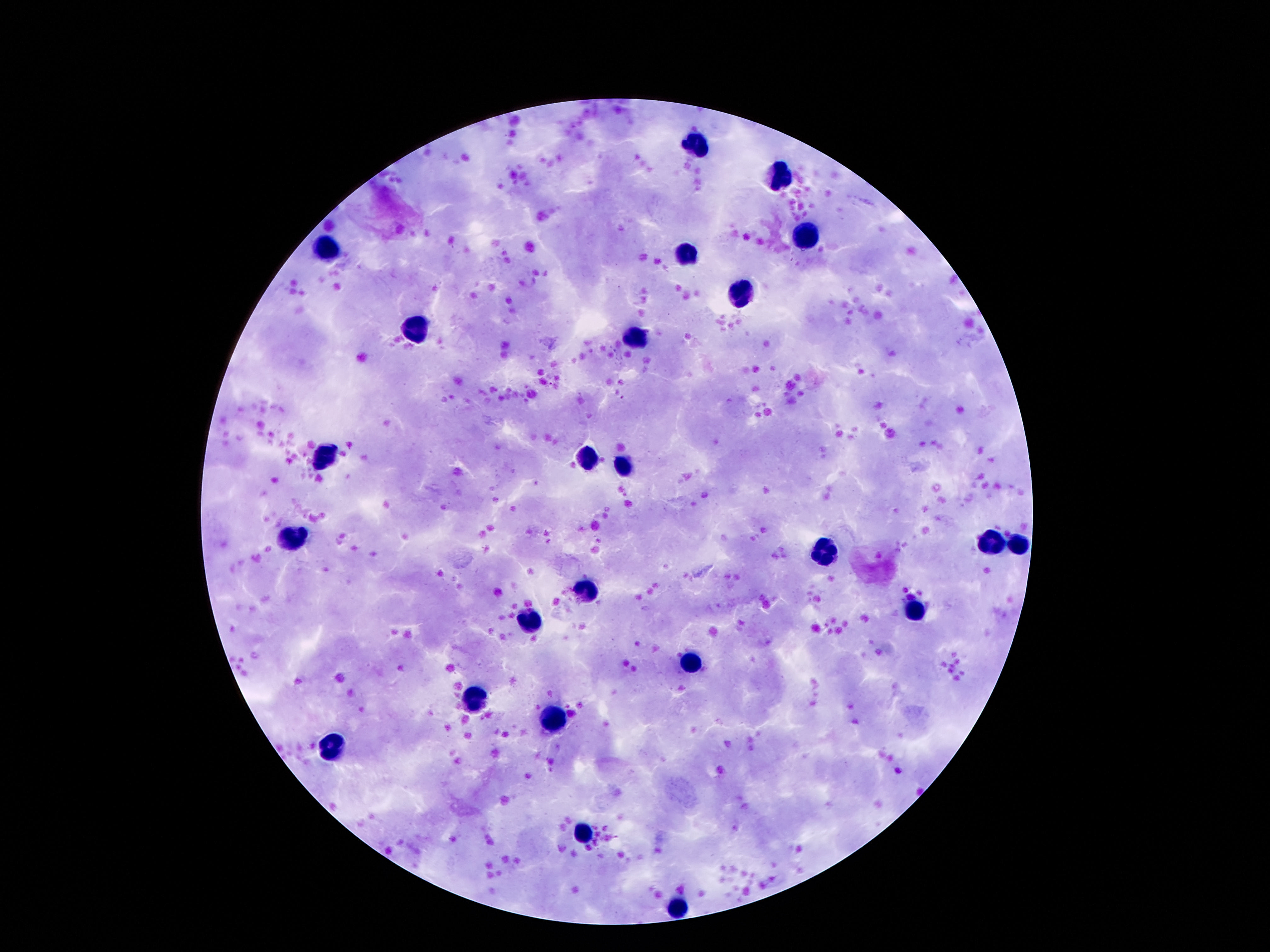

Approximate object centers, in pixels from the top-left corner. Leukocyte locations: (x=694, y=145), (x=773, y=180), (x=808, y=238), (x=323, y=246), (x=683, y=254), (x=743, y=297), (x=412, y=330), (x=637, y=335), (x=325, y=454), (x=588, y=457), (x=624, y=465), (x=290, y=536), (x=995, y=543), (x=1017, y=544), (x=824, y=551), (x=583, y=590), (x=914, y=609), (x=529, y=622), (x=689, y=663), (x=469, y=700), (x=548, y=719), (x=333, y=746), (x=583, y=834), (x=678, y=906). Giemsa-stained preparation. Single field of view. Patient malaria status: uninfected. Image is 1270×952 pixels. 100x magnification. Thick blood film. Smartphone photograph taken through the microscope eyepiece.